Report the malaria status of this cell.
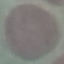
Uninfected.

preparation = thin smear
stain = Giemsa
image type = automatically extracted cell patch, resized to 64 × 64 pixels
capture = smartphone through the microscope eyepiece